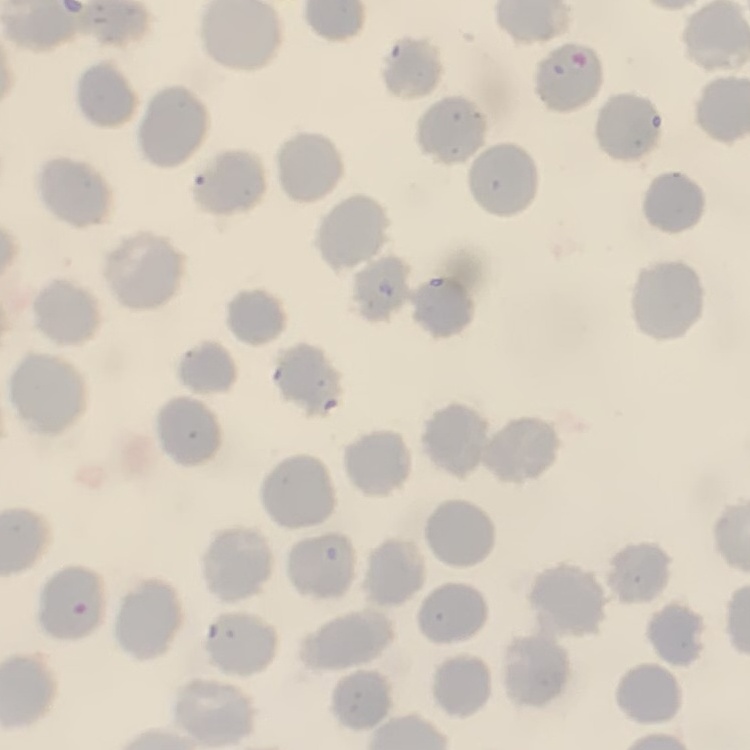
Summary:
  - Erythrocyte morphology: no rouleaux formation
  - Preparation: thin peripheral smear
  - Stain: Field's or Giemsa
  - Image type: one tile cut from a larger photomicrograph